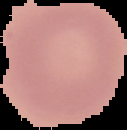

preparation: thin blood smear
image_size: 127×130 pixels
image_type: segmented cell region on a black background
result: no malaria parasites seen